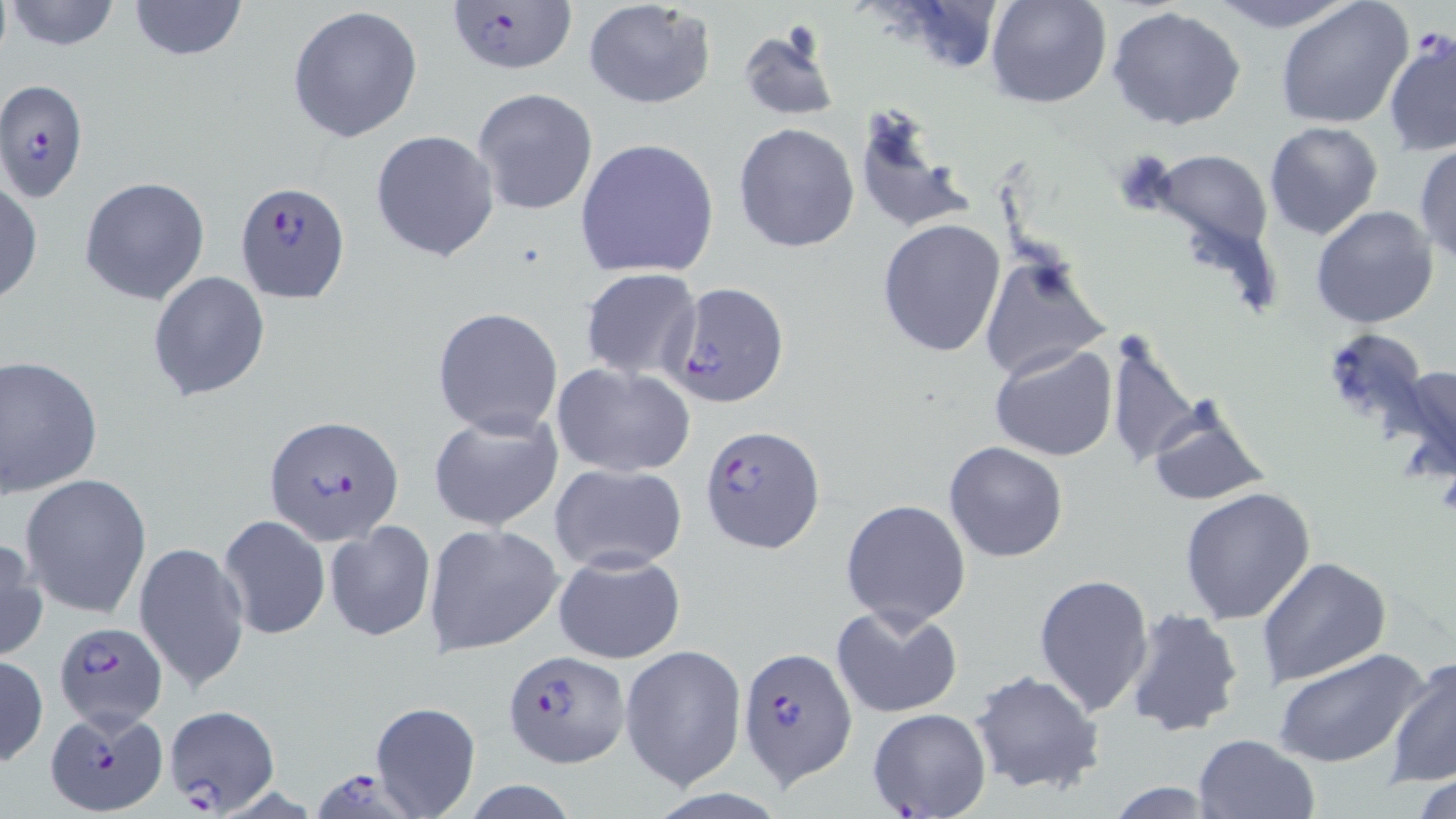

Summary:
  - Coordinate format: approximate bounding boxes as named x1/y1/x2/y2 corners in pixels
  - Platelet locations: (x1=1111, y1=147, x2=1180, y2=218)
  - Plasmodium falciparum-infected red blood cell locations: (x1=443, y1=2, x2=575, y2=78), (x1=0, y1=79, x2=89, y2=203), (x1=234, y1=181, x2=350, y2=302), (x1=664, y1=281, x2=792, y2=409), (x1=266, y1=414, x2=403, y2=542), (x1=699, y1=428, x2=822, y2=559), (x1=51, y1=620, x2=169, y2=729), (x1=737, y1=647, x2=858, y2=787), (x1=505, y1=652, x2=627, y2=767), (x1=46, y1=705, x2=168, y2=815), (x1=160, y1=706, x2=281, y2=815), (x1=315, y1=768, x2=426, y2=819)
  - Uninfected red blood cell locations: (x1=125, y1=0, x2=251, y2=64), (x1=583, y1=0, x2=717, y2=110), (x1=984, y1=0, x2=1113, y2=109), (x1=1210, y1=0, x2=1357, y2=33), (x1=1275, y1=0, x2=1413, y2=129), (x1=4, y1=1, x2=126, y2=51), (x1=287, y1=5, x2=423, y2=143), (x1=1107, y1=6, x2=1248, y2=132), (x1=735, y1=25, x2=841, y2=122), (x1=1383, y1=32, x2=1456, y2=157), (x1=472, y1=88, x2=599, y2=216), (x1=851, y1=103, x2=975, y2=238), (x1=1264, y1=121, x2=1383, y2=241), (x1=732, y1=122, x2=860, y2=254), (x1=370, y1=130, x2=500, y2=263), (x1=573, y1=137, x2=720, y2=279), (x1=1413, y1=144, x2=1456, y2=263), (x1=1149, y1=148, x2=1274, y2=253), (x1=79, y1=175, x2=210, y2=306), (x1=1, y1=178, x2=42, y2=306), (x1=1310, y1=205, x2=1439, y2=330), (x1=876, y1=219, x2=1007, y2=359), (x1=976, y1=255, x2=1112, y2=383), (x1=579, y1=268, x2=702, y2=380), (x1=147, y1=272, x2=273, y2=402), (x1=432, y1=307, x2=564, y2=437), (x1=1325, y1=327, x2=1430, y2=431), (x1=1106, y1=337, x2=1201, y2=469), (x1=989, y1=342, x2=1118, y2=462), (x1=0, y1=355, x2=102, y2=497), (x1=551, y1=362, x2=696, y2=477), (x1=1392, y1=362, x2=1456, y2=478), (x1=1144, y1=394, x2=1272, y2=507), (x1=427, y1=410, x2=566, y2=532), (x1=943, y1=442, x2=1069, y2=563), (x1=547, y1=464, x2=689, y2=574), (x1=20, y1=474, x2=152, y2=619), (x1=1179, y1=485, x2=1318, y2=625), (x1=840, y1=499, x2=971, y2=630), (x1=218, y1=514, x2=330, y2=640), (x1=323, y1=521, x2=434, y2=642), (x1=424, y1=524, x2=563, y2=656), (x1=0, y1=537, x2=47, y2=661), (x1=134, y1=540, x2=250, y2=697), (x1=552, y1=550, x2=686, y2=665), (x1=1256, y1=556, x2=1390, y2=689), (x1=1033, y1=572, x2=1156, y2=718), (x1=831, y1=604, x2=963, y2=719), (x1=1123, y1=607, x2=1246, y2=738), (x1=620, y1=643, x2=747, y2=789), (x1=1274, y1=646, x2=1432, y2=770), (x1=0, y1=653, x2=47, y2=766), (x1=1384, y1=653, x2=1456, y2=788), (x1=969, y1=669, x2=1106, y2=796), (x1=369, y1=701, x2=481, y2=817), (x1=866, y1=708, x2=991, y2=819), (x1=1193, y1=732, x2=1319, y2=818), (x1=1410, y1=772, x2=1456, y2=819), (x1=1102, y1=778, x2=1225, y2=817)
  - Slide-level diagnosis: Plasmodium falciparum
  - Field of view: single
  - Preparation: thin blood smear
  - Magnification: 1000x
  - Stain: May-Grünwald-Giemsa
  - Image size: 1456×819 pixels
  - Modality: light microscopy